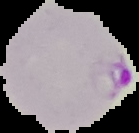
Summary:
  - Image size: 139×133 pixels
  - Image type: segmented cell region on a black background
  - Result: Plasmodium parasites identified
  - Preparation: thin blood smear